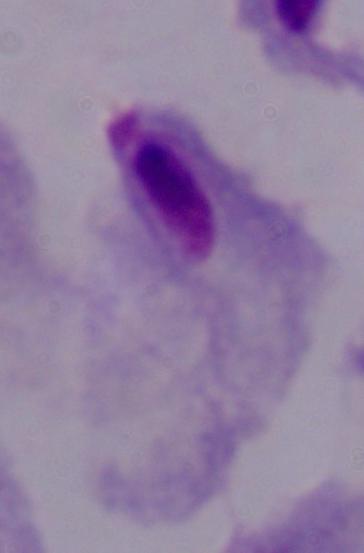
magnification = 1000x
identification = trichomonad
modality = photomicrograph